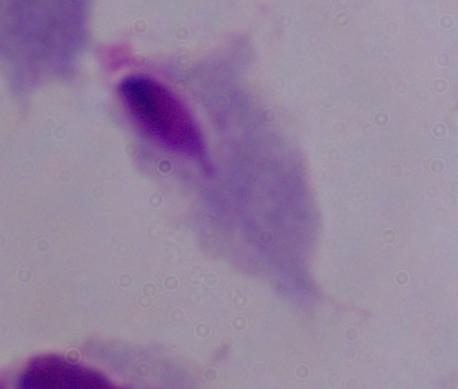
{
  "magnification": "1000x",
  "identification": "trichomonad",
  "modality": "micrograph"
}